Comment on the morphology of the red blood cells.
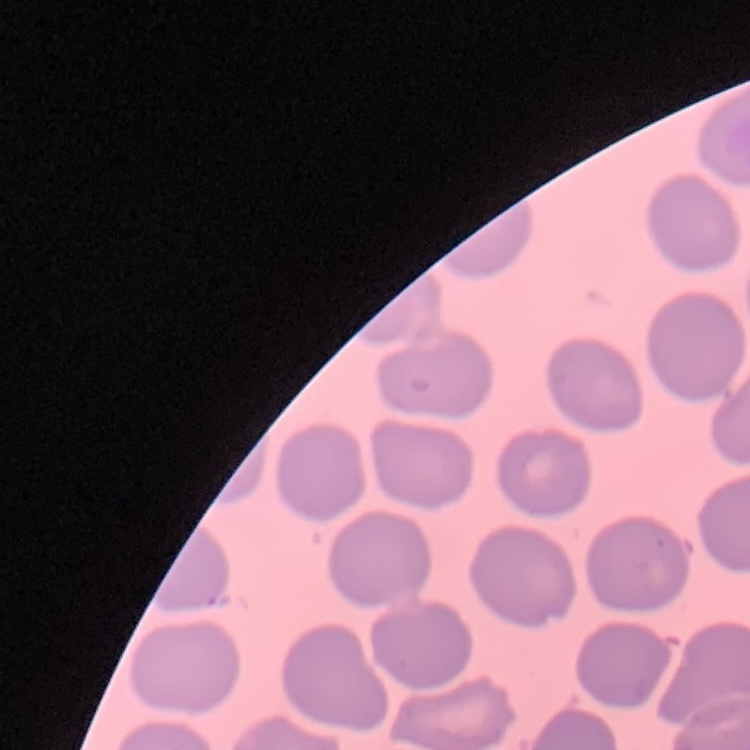
They show no rouleaux formation.

Summary:
  - Preparation: thin blood film
  - Stain: Field's or Giemsa
  - Image type: square crop of a larger photomicrograph